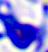
modality = micrograph
magnification = 400x
identification = leukocyte